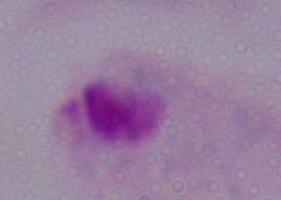

Summary:
  - Modality: micrograph
  - Magnification: 1000x
  - Identification: trichomonad